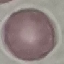
malaria status = uninfected
stain = Giemsa
image type = cell patch, automatically extracted from a larger field of view and resized to 64 × 64 pixels
preparation = thin blood film
capture = smartphone camera at the microscope eyepiece